State which parasite is depicted.
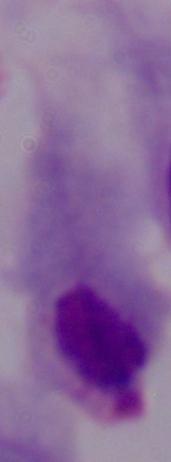
A trichomonad.

Summary:
  - Magnification: 1000x
  - Modality: micrograph